Which red blood cells are Plasmodium falciparum-infected, and which are of indeterminate infection status?
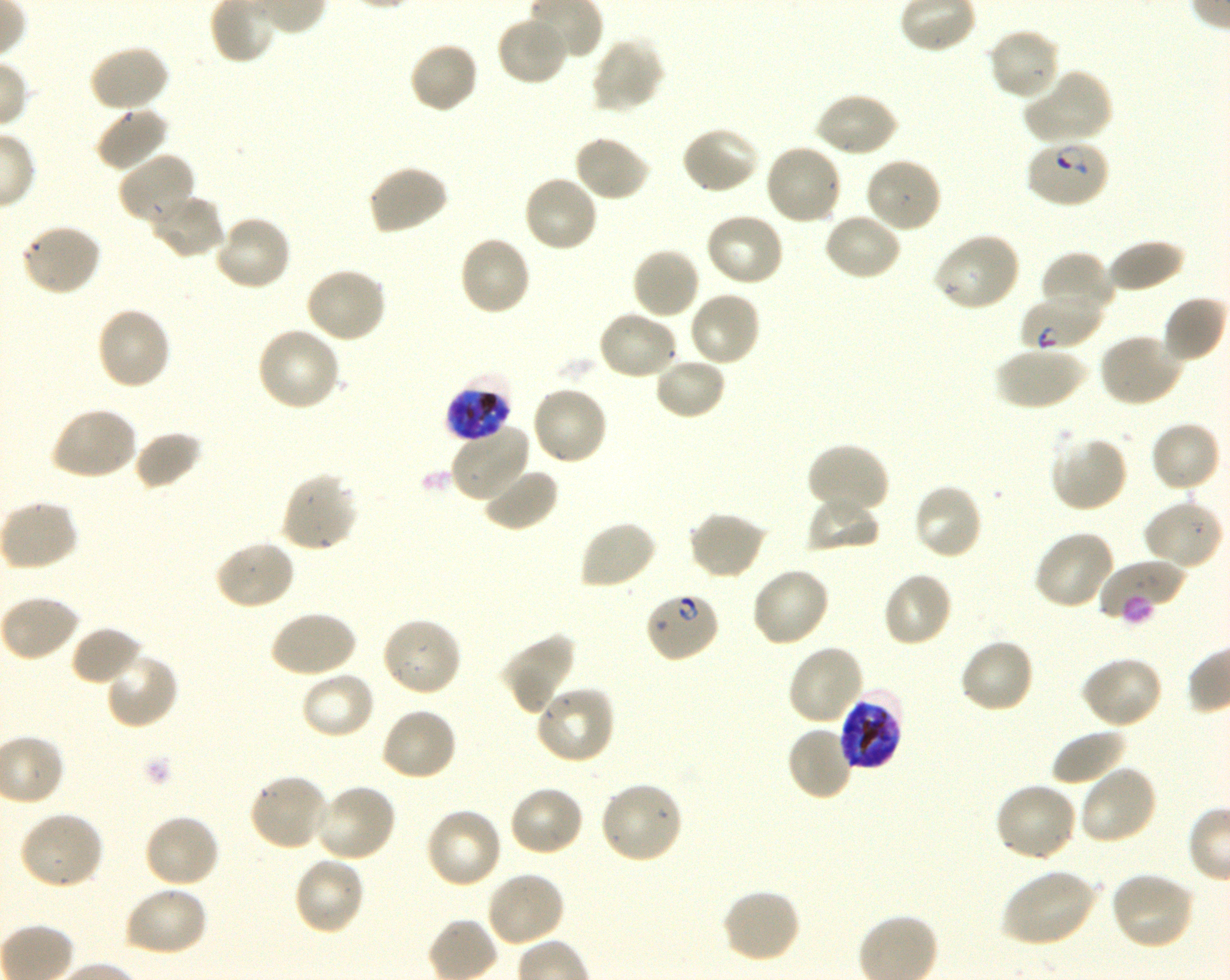

Approximate bounding boxes as {x1, y1, x2, y2} in pixels. Not every red blood cell is marked. A life-cycle stage — or a range of stages, where the recorded stages span more than one — follows each staged infected red blood cell.
Infected red blood cells: {1024, 137, 1111, 208} ring; {1019, 296, 1102, 354} ring; {445, 375, 513, 443} late trophozoite to late schizont; {643, 590, 721, 664} early ring to early trophozoite; {837, 691, 904, 771} late trophozoite to late schizont.
No red blood cells of indeterminate infection status observed.

locations of uninfected red blood cells = {496, 15, 569, 87}, {987, 27, 1062, 102}, {590, 35, 666, 114}, {408, 40, 480, 115}, {88, 44, 171, 114}, {1022, 70, 1113, 147}, {813, 90, 899, 159}, {94, 107, 170, 173}, {679, 126, 761, 196}, {573, 134, 652, 203}, {763, 142, 844, 226}, {117, 152, 198, 228}, {865, 156, 944, 235}, {365, 164, 449, 236}, {522, 173, 600, 254}, {149, 191, 227, 261}, {822, 211, 904, 282}, {704, 212, 786, 289}, {212, 213, 293, 293}, {20, 223, 102, 297}, {932, 231, 1021, 313}, {458, 235, 532, 317}, {1106, 239, 1185, 294}, {631, 246, 702, 320}, {1040, 251, 1115, 321}, {305, 266, 388, 345}, {687, 289, 762, 368}, {1161, 295, 1226, 365}, {94, 305, 173, 392}, {597, 310, 678, 382}, {254, 325, 341, 413}, {1098, 332, 1184, 408}, {994, 346, 1086, 411}, {653, 356, 728, 420}, {530, 385, 609, 467}, {49, 406, 138, 482}, {1149, 420, 1221, 494}, {450, 422, 531, 504}, {132, 430, 202, 490}, {1050, 433, 1129, 513}, {805, 443, 889, 516}, {482, 465, 559, 533}, {278, 473, 359, 553}, {911, 482, 984, 561}, {805, 496, 881, 554}, {1142, 498, 1224, 570}, {0, 499, 79, 571}, {687, 509, 769, 581}, {579, 519, 658, 591}, {1032, 529, 1116, 611}, {213, 539, 296, 610}, {1098, 558, 1185, 621}, {749, 566, 830, 648}, {881, 571, 953, 649}, {0, 595, 82, 663}, {269, 609, 358, 679}, {380, 616, 463, 698}, {69, 625, 144, 687}, {500, 632, 576, 715}, {957, 637, 1035, 714}, {786, 643, 866, 726}, {103, 650, 179, 730}, {1080, 655, 1163, 729}, {299, 670, 377, 740}, {533, 685, 615, 765}, {380, 706, 458, 782}, {785, 724, 856, 803}, {1051, 728, 1129, 787}, {1078, 764, 1159, 846}, {247, 772, 331, 852}, {597, 780, 683, 865}, {992, 781, 1078, 863}, {314, 783, 398, 863}, {507, 784, 585, 858}, {424, 806, 504, 889}, {18, 811, 105, 891}, {142, 813, 221, 889}, {291, 855, 366, 937}, {1000, 868, 1099, 947}, {484, 869, 565, 947}, {1109, 871, 1197, 951}, {124, 885, 209, 958}, {719, 887, 801, 964}
field of view = single
culture = in-vitro Plasmodium falciparum strain 3D7, shaking
image size = 1230×980 pixels
stain = Giemsa
preparation = thin blood smear
donor blood group = O+
objective = 100x, oil immersion, numerical aperture 1.30